Outline each Plasmodium falciparum-infected red blood cell.
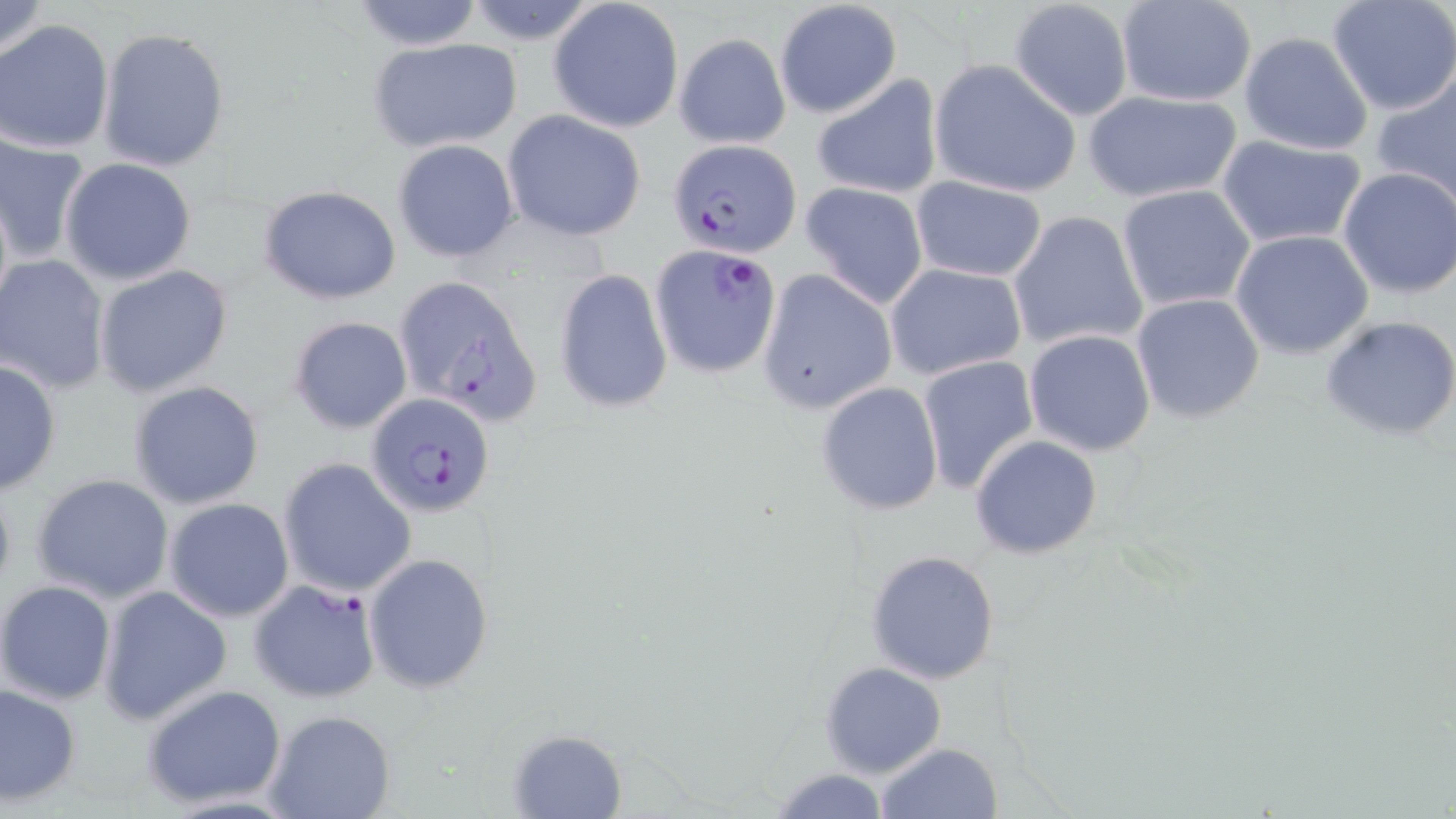
Approximate bounding boxes as [x1, y1, x2, y2] in pixels.
Plasmodium falciparum-infected red blood cells: [669, 139, 801, 258], [650, 242, 783, 380], [393, 275, 539, 422], [367, 393, 494, 517], [247, 579, 382, 705].

Uninfected red blood cell locations: [0, 0, 52, 67], [348, 0, 488, 50], [1326, 0, 1456, 116], [548, 1, 684, 133], [774, 1, 902, 118], [1008, 1, 1134, 120], [1116, 1, 1258, 107], [0, 20, 116, 155], [97, 27, 230, 173], [674, 31, 791, 149], [1238, 32, 1375, 157], [365, 36, 525, 155], [930, 60, 1082, 199], [1372, 72, 1456, 206], [811, 74, 943, 199], [1081, 88, 1242, 203], [502, 112, 646, 241], [1, 134, 93, 264], [1217, 135, 1367, 249], [392, 140, 519, 265], [59, 157, 200, 285], [1335, 167, 1456, 300], [909, 176, 1048, 282], [800, 182, 929, 309], [257, 184, 403, 305], [1116, 184, 1256, 313], [1008, 210, 1149, 352], [1229, 229, 1375, 359], [1, 256, 114, 396], [884, 263, 1026, 381], [94, 264, 235, 398], [553, 269, 674, 414], [758, 270, 898, 415], [1130, 293, 1266, 425], [1321, 314, 1456, 444], [288, 316, 413, 434], [1024, 329, 1156, 456], [916, 356, 1040, 493], [0, 358, 62, 495], [129, 381, 264, 509], [815, 381, 944, 516], [970, 434, 1103, 560], [278, 458, 416, 599], [31, 474, 176, 605], [164, 497, 295, 623], [866, 549, 1002, 685], [363, 553, 494, 692], [1, 580, 117, 706], [96, 585, 234, 726], [820, 662, 947, 778], [0, 681, 81, 808], [141, 684, 289, 809], [263, 710, 398, 819], [507, 728, 626, 817], [874, 742, 1003, 818], [767, 768, 893, 818]. Slide-level diagnosis: Plasmodium falciparum. May-Grünwald-Giemsa stain. Image is 1456×819 pixels. Thin blood smear. Light microscopy. 1000x magnification. One field of a larger specimen.